Assess this cell for malaria.
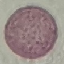
Uninfected.

image type = automatically extracted cell patch, resized to 64 × 64 pixels
capture = smartphone through the microscope eyepiece
stain = Giemsa
preparation = thin blood film